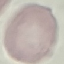
Result: negative for malaria parasites. Giemsa-stained preparation. Automatically extracted cell patch, resized to 64 × 64 pixels. Thin blood film. Acquired by smartphone through the microscope eyepiece.